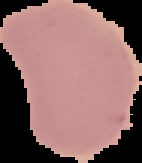

malaria status = uninfected
preparation = thin blood smear
image size = 142×163 pixels
image type = segmented cell region on a black background